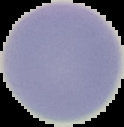
Summary:
  - Preparation: thin blood film
  - Result: negative for malaria parasites
  - Image type: segmented cell region on a black background
  - Image size: 124×127 pixels